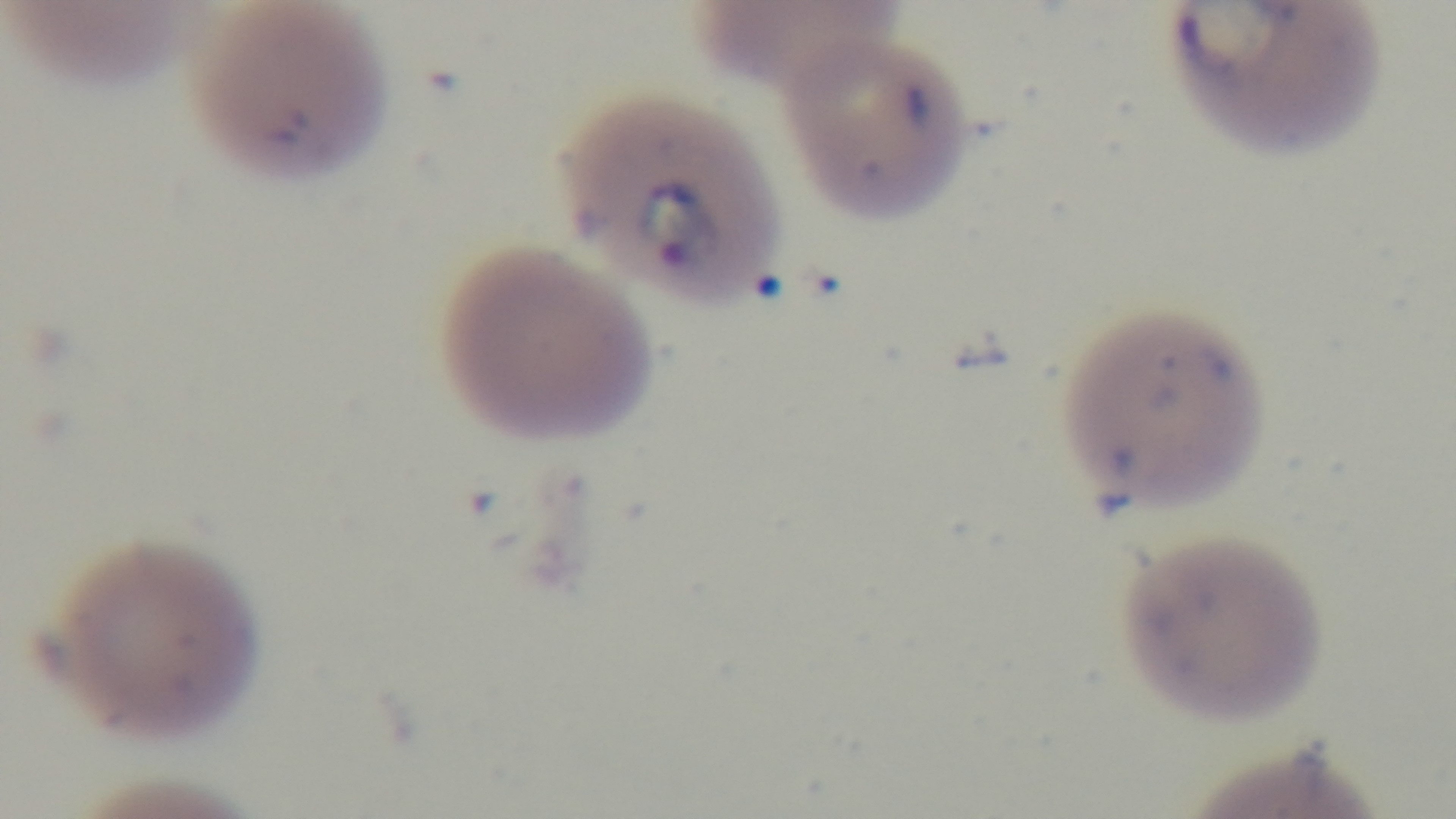 Giemsa-stained. Preparation: thin. Oil-immersion objective, 100x. Light microscopy. One field from the slide. Malaria status: positive. Captured with a mounted 4K digital camera.